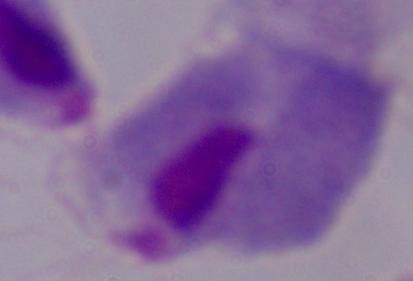
Summary:
  - Modality: photomicrograph
  - Magnification: 1000x
  - Identification: trichomonad